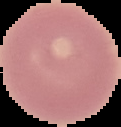

result = no Plasmodium parasites seen
preparation = thin blood smear
image type = cell region segmented out of the field of view; surrounding area masked to black
image size = 121×127 pixels